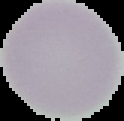
{
  "malaria_status": "uninfected",
  "image_type": "cell region segmented out of the field of view; surrounding area masked to black",
  "preparation": "thin blood film",
  "image_size": "124×121 pixels"
}